Give the position of every leukocyte visible.
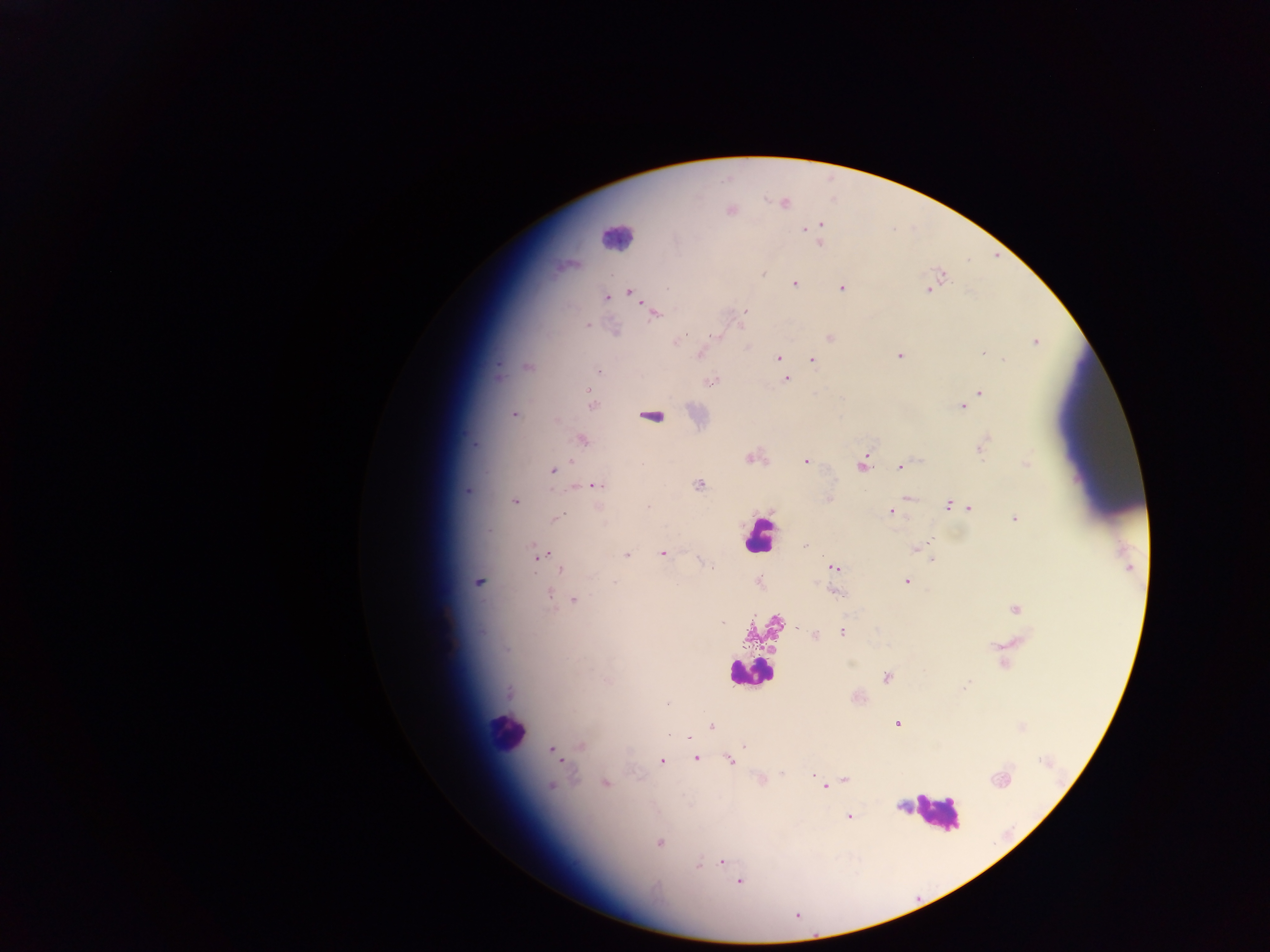

Approximate centers as {x, y} in pixels.
Leukocytes: {618, 238}, {759, 537}, {752, 668}, {510, 735}, {935, 814}.

Malaria parasite locations: {732, 211}, {820, 225}, {804, 227}, {676, 241}, {821, 243}, {764, 274}, {796, 282}, {931, 287}, {628, 290}, {840, 290}, {928, 291}, {607, 298}, {744, 310}, {652, 312}, {741, 324}, {589, 325}, {615, 330}, {717, 335}, {829, 337}, {675, 342}, {1036, 343}, {983, 352}, {701, 353}, {898, 355}, {778, 358}, {812, 359}, {1004, 359}, {598, 370}, {499, 376}, {786, 378}, {709, 382}, {979, 392}, {592, 402}, {969, 403}, {961, 407}, {513, 414}, {986, 440}, {749, 457}, {805, 462}, {1025, 463}, {863, 466}, {898, 467}, {552, 471}, {594, 485}, {698, 485}, {465, 490}, {908, 496}, {829, 497}, {516, 502}, {646, 504}, {946, 504}, {970, 509}, {891, 512}, {559, 516}, {1012, 517}, {930, 540}, {913, 549}, {663, 552}, {551, 553}, {626, 554}, {540, 556}, {931, 560}, {711, 565}, {833, 566}, {560, 570}, {907, 580}, {479, 582}, {613, 582}, {834, 591}, {550, 592}, {574, 598}, {1013, 609}, {844, 632}, {814, 636}, {992, 645}, {850, 663}, {885, 677}, {966, 684}, {510, 692}, {667, 704}, {897, 724}, {710, 726}, {579, 745}, {550, 749}, {695, 758}, {662, 761}, {730, 761}, {782, 772}, {573, 773}, {812, 774}, {845, 779}, {762, 780}, {606, 782}, {550, 786}, {823, 788}, {899, 806}, {848, 817}, {660, 843}, {721, 862}, {697, 868}, {739, 882}. One field of view. Image is 1270×952 pixels. Thick blood film. Photographed through a microscope with a mobile-phone camera. Sample from Ghana.